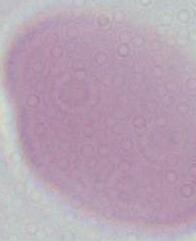

Summary:
  - Modality: photomicrograph
  - Identification: erythrocyte
  - Magnification: 1000x